Assess for Plasmodium parasites.
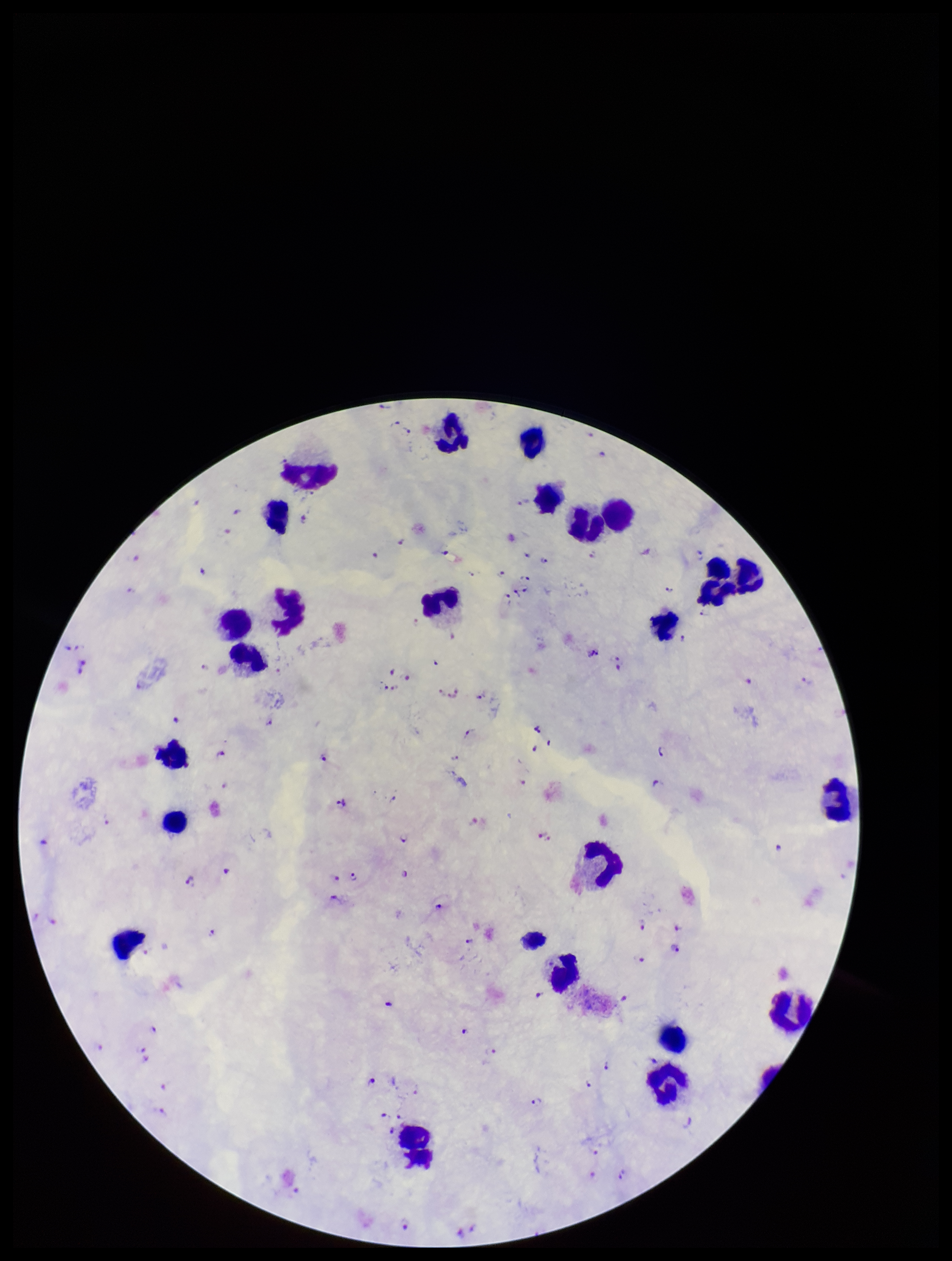
Detected.

parasite_count: 110
patient_malaria_status: positive
leukocyte_count: 26
image_size: 952×1261 pixels
species_reported_for_this_patient: Plasmodium falciparum
stain: Giemsa
preparation: thick smear
capture: smartphone photograph through the microscope eyepiece
field_of_view: single